State which parasite is depicted.
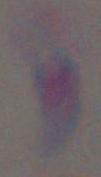
Toxoplasma gondii.

Summary:
  - Magnification: 1000x
  - Modality: photomicrograph